Report the malaria status of this cell.
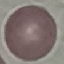
It is uninfected.

Summary:
  - Stain: Giemsa
  - Preparation: thin smear
  - Image type: cell patch, automatically extracted from a larger field of view and resized to 64 × 64 pixels
  - Capture: smartphone camera at the microscope eyepiece